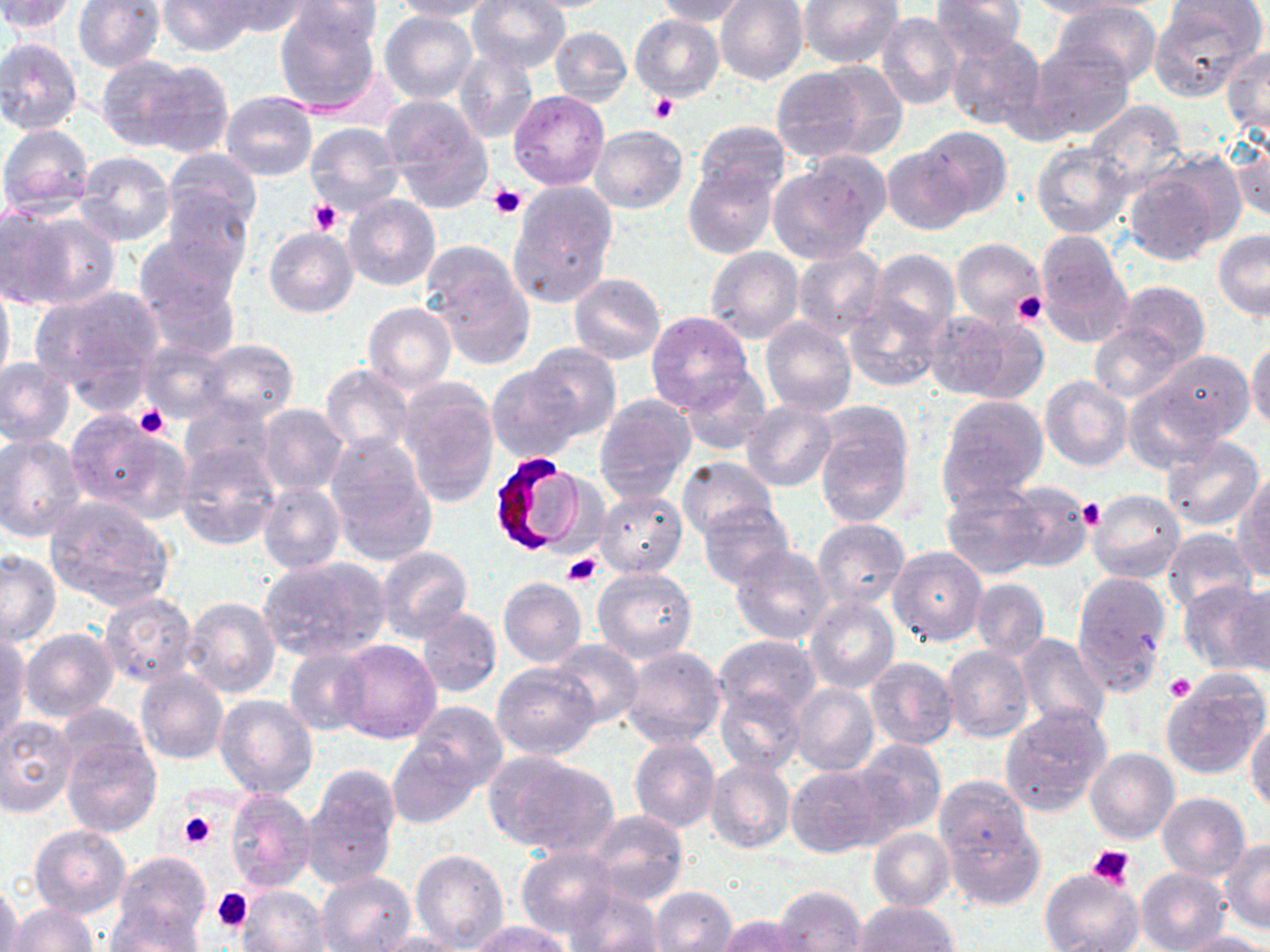

slide-level diagnosis = Plasmodium falciparum
stain = May-Grünwald-Giemsa
preparation = thin blood smear
magnification = 1000x
platelet locations = approximate bounding boxes as named x1/y1/x2/y2 corners in pixels: (x1=650, y1=93, x2=678, y2=122), (x1=488, y1=185, x2=526, y2=218), (x1=310, y1=199, x2=343, y2=235), (x1=1012, y1=293, x2=1048, y2=326), (x1=132, y1=404, x2=174, y2=440), (x1=1078, y1=497, x2=1103, y2=530), (x1=563, y1=552, x2=602, y2=588), (x1=1165, y1=673, x2=1195, y2=701), (x1=178, y1=811, x2=216, y2=851), (x1=1087, y1=841, x2=1136, y2=889), (x1=212, y1=887, x2=254, y2=932)
Plasmodium falciparum-infected red blood cell locations = approximate bounding boxes as named x1/y1/x2/y2 corners in pixels: (x1=484, y1=451, x2=590, y2=560)
uninfected red blood cell locations = approximate bounding boxes as named x1/y1/x2/y2 corners in pixels: (x1=1, y1=0, x2=79, y2=34), (x1=73, y1=0, x2=166, y2=72), (x1=157, y1=0, x2=253, y2=56), (x1=213, y1=0, x2=311, y2=38), (x1=468, y1=0, x2=570, y2=73), (x1=511, y1=0, x2=623, y2=12), (x1=653, y1=0, x2=753, y2=26), (x1=928, y1=0, x2=1028, y2=62), (x1=290, y1=1, x2=385, y2=47), (x1=389, y1=1, x2=493, y2=22), (x1=715, y1=1, x2=808, y2=85), (x1=797, y1=1, x2=904, y2=70), (x1=1014, y1=1, x2=1140, y2=19), (x1=1049, y1=2, x2=1163, y2=90), (x1=1149, y1=3, x2=1264, y2=99), (x1=272, y1=5, x2=383, y2=117), (x1=379, y1=10, x2=478, y2=105), (x1=876, y1=11, x2=963, y2=110), (x1=631, y1=15, x2=724, y2=100), (x1=550, y1=26, x2=632, y2=107), (x1=942, y1=31, x2=1047, y2=132), (x1=0, y1=37, x2=84, y2=135), (x1=1028, y1=42, x2=1134, y2=142), (x1=452, y1=48, x2=538, y2=146), (x1=1222, y1=48, x2=1270, y2=141), (x1=96, y1=54, x2=195, y2=149), (x1=140, y1=61, x2=234, y2=159), (x1=769, y1=64, x2=885, y2=163), (x1=509, y1=90, x2=610, y2=190), (x1=220, y1=91, x2=318, y2=182), (x1=379, y1=95, x2=493, y2=209), (x1=1084, y1=100, x2=1187, y2=194), (x1=693, y1=119, x2=791, y2=200), (x1=303, y1=121, x2=404, y2=215), (x1=0, y1=124, x2=95, y2=217), (x1=589, y1=125, x2=688, y2=213), (x1=913, y1=127, x2=1012, y2=220), (x1=1229, y1=132, x2=1269, y2=225), (x1=1031, y1=142, x2=1132, y2=239), (x1=882, y1=144, x2=976, y2=236), (x1=162, y1=148, x2=263, y2=237), (x1=72, y1=151, x2=175, y2=248), (x1=767, y1=159, x2=885, y2=264), (x1=1124, y1=163, x2=1229, y2=267), (x1=684, y1=165, x2=777, y2=258), (x1=507, y1=180, x2=617, y2=309), (x1=164, y1=186, x2=252, y2=278), (x1=343, y1=195, x2=440, y2=292), (x1=4, y1=206, x2=112, y2=315), (x1=265, y1=227, x2=358, y2=318), (x1=1213, y1=230, x2=1270, y2=320), (x1=1034, y1=232, x2=1133, y2=347), (x1=134, y1=234, x2=238, y2=320), (x1=951, y1=239, x2=1045, y2=328), (x1=706, y1=246, x2=804, y2=343), (x1=791, y1=246, x2=888, y2=340), (x1=867, y1=249, x2=959, y2=338), (x1=427, y1=254, x2=538, y2=369), (x1=569, y1=273, x2=665, y2=364), (x1=0, y1=275, x2=15, y2=392), (x1=143, y1=280, x2=240, y2=362), (x1=1113, y1=280, x2=1210, y2=366), (x1=33, y1=284, x2=166, y2=400), (x1=843, y1=294, x2=947, y2=393), (x1=362, y1=303, x2=456, y2=394), (x1=647, y1=310, x2=752, y2=413), (x1=925, y1=310, x2=1029, y2=402), (x1=759, y1=317, x2=857, y2=417), (x1=1089, y1=323, x2=1184, y2=403), (x1=137, y1=338, x2=234, y2=424), (x1=1247, y1=338, x2=1270, y2=433), (x1=195, y1=339, x2=299, y2=424), (x1=524, y1=342, x2=622, y2=439), (x1=1141, y1=348, x2=1253, y2=448), (x1=0, y1=359, x2=74, y2=447), (x1=487, y1=364, x2=582, y2=463), (x1=320, y1=365, x2=416, y2=457), (x1=679, y1=368, x2=772, y2=455), (x1=1039, y1=375, x2=1132, y2=471), (x1=398, y1=379, x2=499, y2=507), (x1=1123, y1=384, x2=1221, y2=473), (x1=594, y1=394, x2=696, y2=501), (x1=936, y1=395, x2=1048, y2=508), (x1=179, y1=401, x2=275, y2=488), (x1=740, y1=402, x2=837, y2=492), (x1=256, y1=404, x2=350, y2=495), (x1=813, y1=405, x2=916, y2=528), (x1=66, y1=412, x2=189, y2=522), (x1=0, y1=435, x2=86, y2=541), (x1=325, y1=435, x2=437, y2=561), (x1=1160, y1=435, x2=1265, y2=532), (x1=175, y1=441, x2=280, y2=549), (x1=675, y1=456, x2=778, y2=542), (x1=1233, y1=479, x2=1270, y2=581), (x1=998, y1=480, x2=1092, y2=572), (x1=258, y1=481, x2=345, y2=574), (x1=941, y1=483, x2=1048, y2=579), (x1=1086, y1=488, x2=1185, y2=582), (x1=596, y1=489, x2=688, y2=578), (x1=46, y1=498, x2=174, y2=611), (x1=697, y1=501, x2=795, y2=591), (x1=813, y1=518, x2=909, y2=611), (x1=1162, y1=528, x2=1260, y2=614), (x1=730, y1=544, x2=834, y2=645), (x1=888, y1=544, x2=988, y2=647), (x1=375, y1=546, x2=472, y2=643), (x1=0, y1=549, x2=61, y2=646), (x1=260, y1=555, x2=391, y2=661), (x1=592, y1=565, x2=697, y2=662), (x1=1072, y1=572, x2=1172, y2=691), (x1=498, y1=578, x2=587, y2=669), (x1=970, y1=579, x2=1049, y2=661), (x1=1179, y1=580, x2=1270, y2=675), (x1=1233, y1=582, x2=1269, y2=678), (x1=99, y1=593, x2=198, y2=686), (x1=182, y1=595, x2=281, y2=697), (x1=804, y1=595, x2=900, y2=694), (x1=416, y1=608, x2=502, y2=698), (x1=21, y1=627, x2=118, y2=722), (x1=1013, y1=633, x2=1110, y2=731), (x1=0, y1=634, x2=31, y2=744), (x1=712, y1=634, x2=822, y2=725), (x1=334, y1=640, x2=441, y2=744), (x1=547, y1=640, x2=643, y2=728), (x1=619, y1=643, x2=728, y2=749), (x1=942, y1=645, x2=1034, y2=742), (x1=285, y1=646, x2=373, y2=735), (x1=864, y1=657, x2=959, y2=750), (x1=492, y1=662, x2=600, y2=758), (x1=136, y1=670, x2=228, y2=765), (x1=792, y1=674, x2=954, y2=762), (x1=1162, y1=674, x2=1269, y2=779), (x1=789, y1=683, x2=879, y2=777), (x1=715, y1=689, x2=803, y2=775), (x1=213, y1=695, x2=318, y2=799), (x1=411, y1=701, x2=509, y2=791), (x1=1000, y1=703, x2=1113, y2=816), (x1=0, y1=716, x2=77, y2=816), (x1=1246, y1=717, x2=1270, y2=814), (x1=59, y1=731, x2=162, y2=839), (x1=629, y1=737, x2=721, y2=832), (x1=388, y1=738, x2=480, y2=829), (x1=851, y1=738, x2=946, y2=838), (x1=1085, y1=747, x2=1179, y2=845), (x1=484, y1=750, x2=619, y2=858), (x1=706, y1=759, x2=795, y2=853), (x1=786, y1=763, x2=893, y2=857), (x1=303, y1=769, x2=399, y2=887), (x1=933, y1=775, x2=1032, y2=863), (x1=225, y1=789, x2=316, y2=892), (x1=1156, y1=793, x2=1250, y2=880), (x1=588, y1=811, x2=688, y2=904), (x1=942, y1=814, x2=1045, y2=911), (x1=30, y1=825, x2=130, y2=919), (x1=867, y1=827, x2=954, y2=911), (x1=580, y1=830, x2=713, y2=946), (x1=1219, y1=841, x2=1270, y2=934), (x1=516, y1=847, x2=618, y2=939), (x1=409, y1=849, x2=509, y2=951), (x1=116, y1=851, x2=211, y2=947), (x1=1136, y1=867, x2=1231, y2=951), (x1=1039, y1=868, x2=1143, y2=952), (x1=317, y1=871, x2=417, y2=951), (x1=0, y1=883, x2=22, y2=952), (x1=562, y1=883, x2=666, y2=952), (x1=772, y1=884, x2=868, y2=951), (x1=235, y1=885, x2=329, y2=952), (x1=649, y1=886, x2=738, y2=952), (x1=851, y1=900, x2=960, y2=951), (x1=8, y1=903, x2=97, y2=952), (x1=105, y1=904, x2=206, y2=952), (x1=719, y1=915, x2=811, y2=952), (x1=468, y1=921, x2=570, y2=952), (x1=365, y1=930, x2=477, y2=952), (x1=1172, y1=931, x2=1270, y2=951)
modality = optical microscopy
field of view = one of a larger specimen
image size = 1270×952 pixels